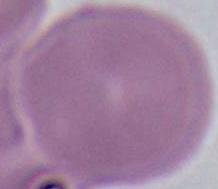
identification = red blood cell
magnification = 1000x
modality = photomicrograph